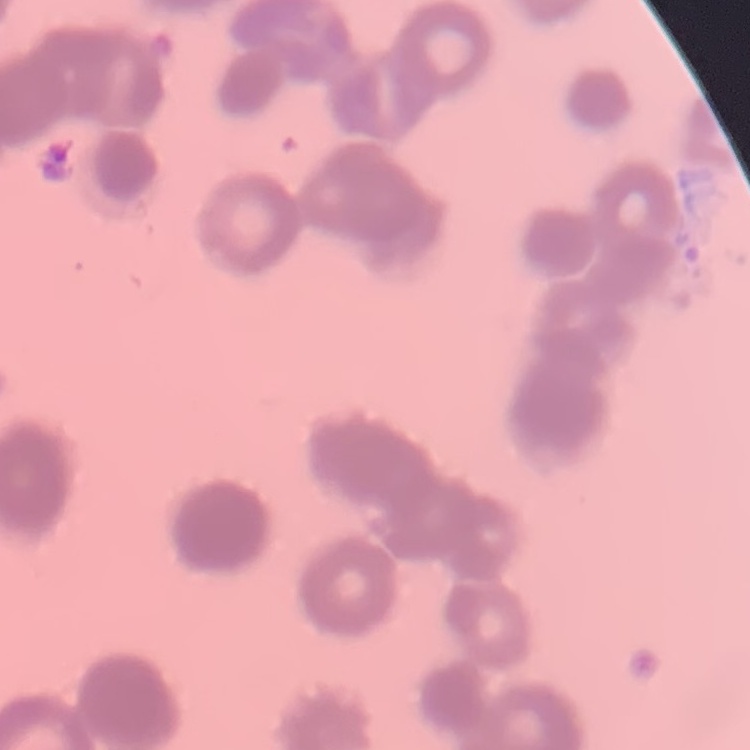
Summary:
  - Red blood cell morphology: rouleaux formation
  - Stain: Field's or Giemsa
  - Preparation: thin peripheral smear
  - Image type: square crop of a larger photomicrograph